Locate every Plasmodium parasite.
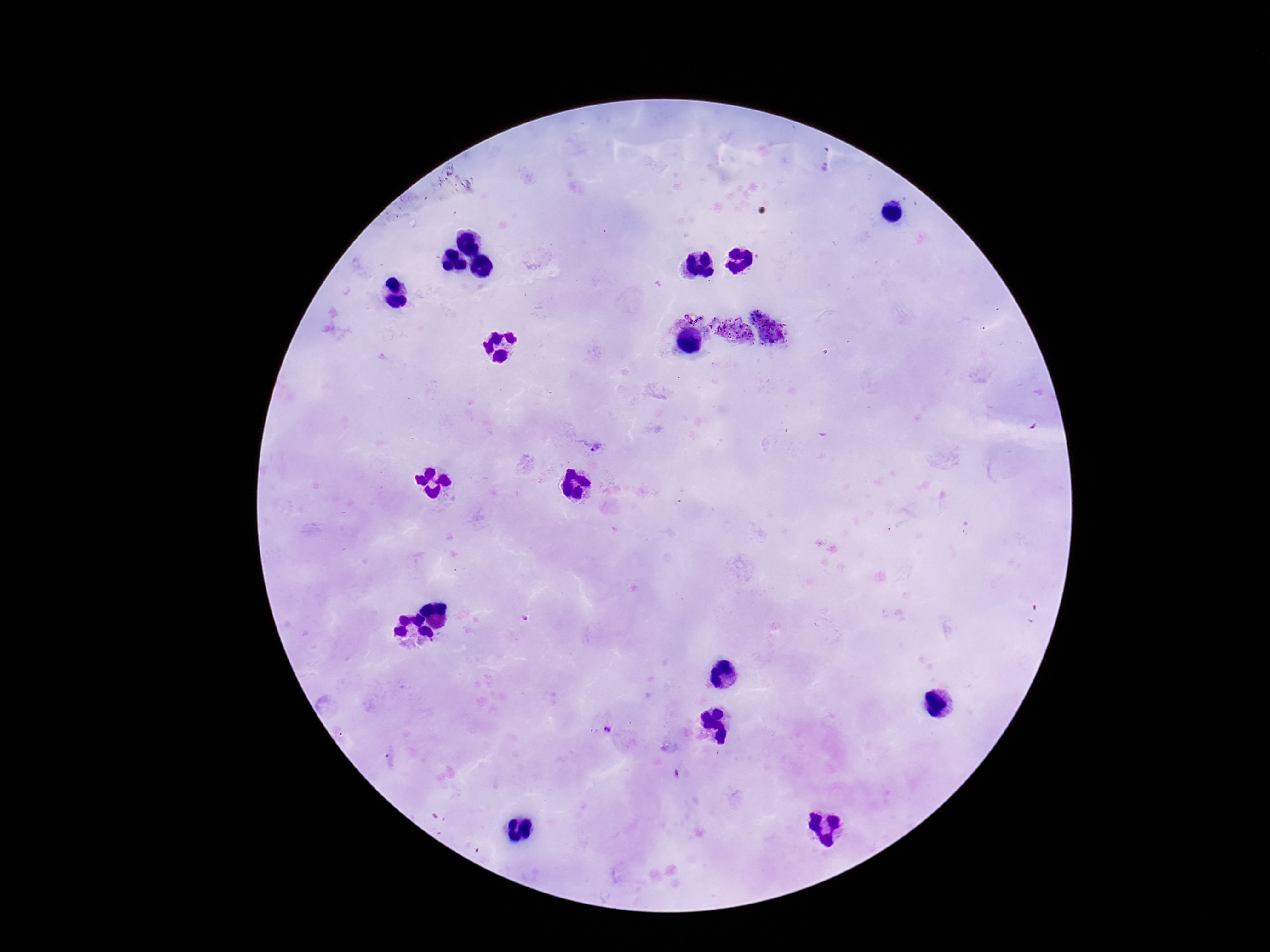
Approximate object centers, in pixels from the top-left corner.
Plasmodium parasites: (x=597, y=448), (x=606, y=731).

Summary:
  - Field of view: one from this slide
  - Image size: 1270×952 pixels
  - Capture: smartphone camera through the microscope eyepiece
  - Magnification: 100x
  - Patient malaria status: positive
  - Preparation: thick blood film
  - Stain: Giemsa